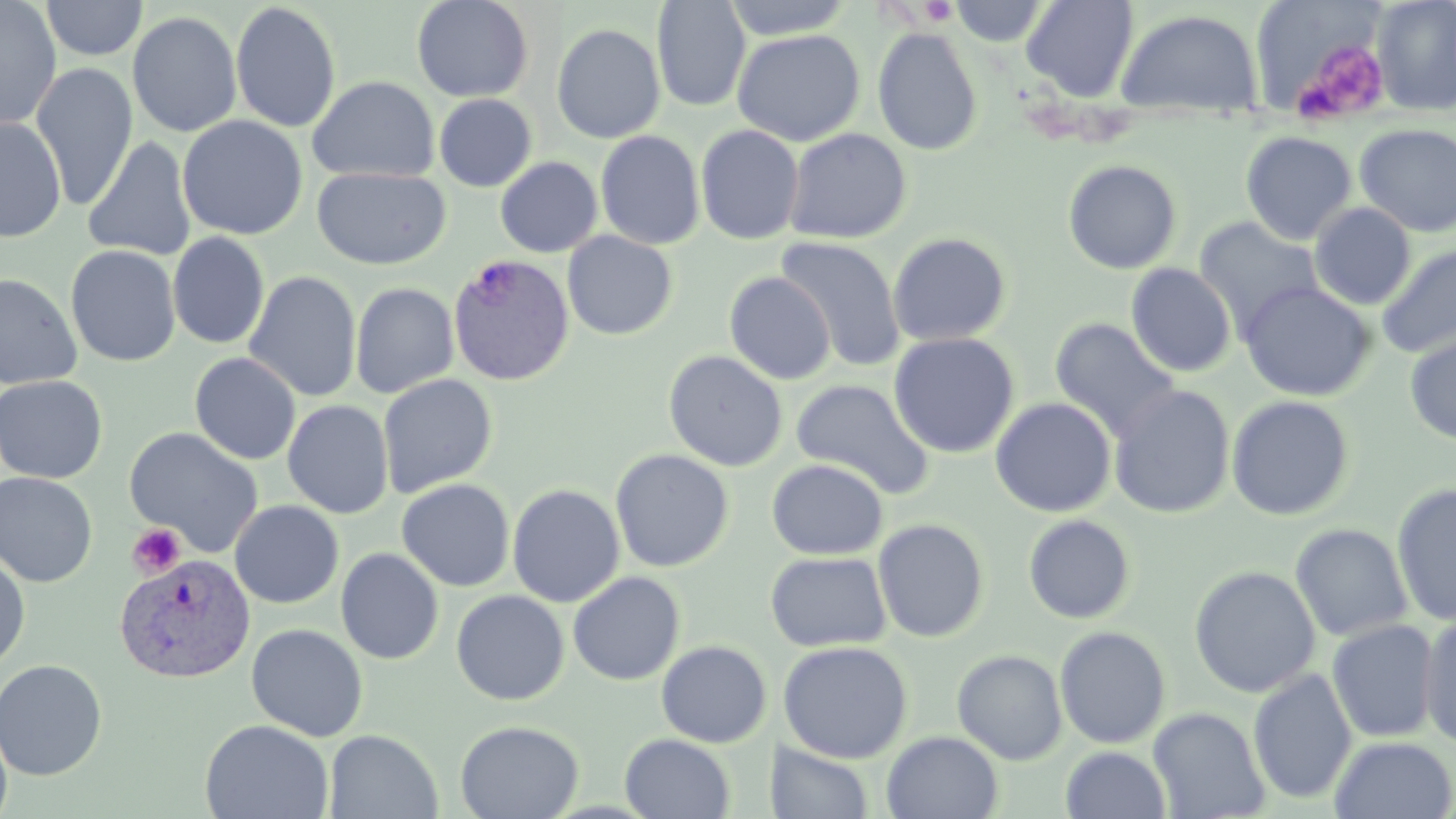

slide_level_diagnosis: Plasmodium vivax
magnification: 1000x
platelet_locations: 'approximate bounding boxes as [x1, y1, x2, y2] in pixels: [919, 1, 959, 25], [1293, 40, 1391, 126], [126, 522, 186, 579]'
image_size: 1456×819 pixels
plasmodium_vivax_infected_red_blood_cell_locations: 'approximate bounding boxes as [x1, y1, x2, y2] in pixels: [449, 253, 574, 385], [115, 552, 256, 683]'
field_of_view: single
uninfected_red_blood_cell_locations: 'approximate bounding boxes as [x1, y1, x2, y2] in pixels: [41, 0, 148, 61], [411, 0, 534, 102], [721, 0, 858, 39], [949, 0, 1049, 46], [1021, 0, 1139, 101], [1371, 0, 1456, 116], [0, 1, 61, 131], [652, 1, 751, 112], [230, 2, 342, 133], [1251, 5, 1382, 115], [1115, 9, 1264, 118], [127, 11, 243, 138], [552, 23, 666, 144], [873, 28, 983, 156], [732, 29, 865, 146], [30, 63, 138, 211], [307, 75, 439, 183], [434, 94, 537, 192], [177, 115, 308, 240], [0, 116, 67, 243], [1355, 122, 1456, 236], [695, 124, 805, 244], [783, 128, 911, 244], [596, 130, 705, 250], [1240, 131, 1356, 244], [84, 136, 197, 262], [495, 156, 603, 258], [1062, 159, 1182, 274], [312, 167, 451, 269], [1309, 202, 1417, 310], [1194, 218, 1324, 332], [562, 231, 678, 340], [168, 232, 270, 349], [887, 232, 1012, 347], [774, 236, 908, 372], [1217, 239, 1355, 367], [65, 244, 181, 367], [1376, 244, 1456, 360], [1126, 263, 1237, 377], [243, 271, 361, 402], [724, 271, 837, 385], [0, 272, 83, 390], [1239, 281, 1376, 401], [350, 282, 459, 399], [1049, 317, 1180, 440], [888, 332, 1020, 458], [1405, 333, 1456, 445], [663, 350, 787, 472], [190, 352, 301, 465], [377, 373, 498, 498], [0, 375, 108, 484], [791, 379, 934, 499], [1108, 384, 1236, 518], [1226, 395, 1356, 521], [990, 397, 1117, 517], [282, 400, 394, 518], [124, 427, 264, 558], [610, 448, 734, 573], [766, 459, 888, 560], [0, 471, 98, 588], [397, 478, 515, 592], [1392, 482, 1456, 626], [507, 483, 626, 607], [229, 500, 344, 608], [1022, 514, 1136, 624], [872, 518, 990, 643], [1290, 523, 1413, 642], [336, 548, 444, 664], [765, 551, 892, 652], [0, 552, 30, 670], [1189, 565, 1321, 698], [568, 571, 685, 686], [451, 590, 569, 705], [1419, 616, 1456, 749], [1326, 619, 1441, 742], [246, 623, 368, 741], [1054, 626, 1171, 749], [656, 640, 771, 748], [777, 640, 913, 763], [952, 649, 1068, 765], [0, 659, 108, 780], [1248, 669, 1357, 805], [1148, 707, 1270, 819], [0, 716, 13, 819], [200, 719, 334, 819], [455, 720, 583, 819], [324, 729, 443, 819], [881, 731, 1003, 819], [619, 733, 735, 818], [1328, 735, 1456, 819], [775, 742, 874, 819], [1061, 746, 1172, 819]'
preparation: thin blood film
modality: light microscopy
stain: May-Grünwald-Giemsa